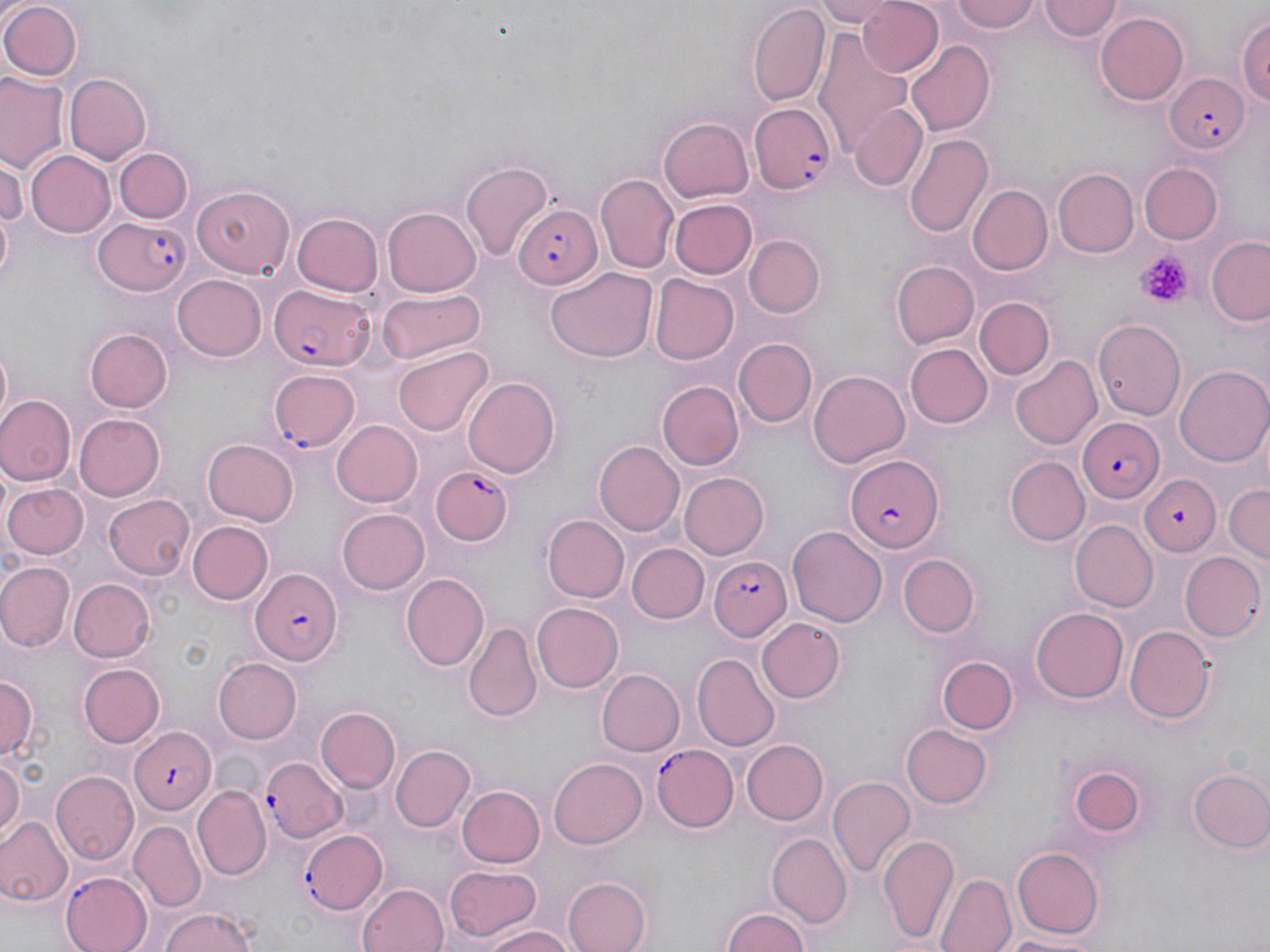 Approximate bounding boxes as (x1, y1, x2, y2) in pixels. Plasmodium falciparum-infected red blood cell locations: (1165, 71, 1251, 156), (750, 102, 837, 196), (512, 203, 600, 289), (93, 217, 191, 296), (270, 286, 373, 370), (268, 369, 361, 451), (1075, 415, 1164, 501), (843, 453, 945, 553), (428, 464, 514, 548), (710, 557, 793, 642), (248, 566, 340, 666), (126, 726, 217, 815), (650, 743, 739, 833), (263, 756, 349, 842), (298, 827, 389, 915). Uninfected red blood cell locations: (812, 0, 899, 26), (855, 0, 943, 77), (947, 0, 1040, 35), (1036, 0, 1124, 41), (0, 1, 81, 82), (747, 4, 831, 107), (1238, 12, 1270, 114), (1094, 13, 1190, 105), (814, 32, 911, 157), (905, 39, 995, 135), (0, 73, 66, 173), (64, 73, 150, 165), (849, 103, 926, 192), (659, 115, 754, 204), (904, 133, 994, 240), (112, 144, 192, 226), (26, 150, 115, 237), (0, 157, 25, 232), (461, 161, 553, 261), (1138, 163, 1223, 245), (1055, 168, 1139, 258), (596, 173, 679, 274), (192, 183, 297, 278), (966, 184, 1054, 276), (669, 199, 756, 279), (382, 207, 483, 295), (294, 213, 383, 297), (744, 235, 826, 317), (1207, 236, 1270, 326), (892, 260, 978, 349), (545, 267, 658, 363), (649, 272, 739, 365), (171, 273, 265, 361), (378, 287, 486, 364), (974, 296, 1053, 381), (1093, 318, 1187, 422), (85, 327, 172, 413), (733, 338, 817, 428), (1, 339, 14, 429), (906, 344, 993, 428), (392, 347, 491, 437), (1010, 355, 1101, 450), (1175, 366, 1270, 467), (811, 369, 908, 468), (462, 375, 562, 478), (659, 380, 742, 469), (0, 396, 75, 485), (74, 412, 164, 499), (333, 421, 421, 507), (202, 437, 298, 525), (595, 440, 685, 537), (1007, 456, 1091, 545), (678, 471, 769, 559), (1138, 475, 1223, 557), (2, 483, 88, 560), (1225, 483, 1269, 562), (105, 493, 196, 580), (336, 508, 430, 595), (543, 515, 627, 603), (187, 520, 272, 605), (1071, 520, 1157, 611), (788, 525, 887, 627), (629, 543, 708, 624), (1182, 551, 1266, 641), (900, 554, 977, 637), (0, 563, 74, 651), (400, 573, 489, 672), (69, 579, 155, 661), (532, 602, 624, 692), (1032, 605, 1130, 701), (756, 617, 847, 703), (462, 621, 542, 724), (1123, 625, 1215, 726), (692, 653, 780, 749), (937, 653, 1019, 734), (213, 657, 303, 743), (78, 662, 165, 747), (596, 669, 684, 756), (0, 672, 39, 760), (316, 707, 400, 794), (901, 723, 992, 808), (741, 738, 828, 825), (391, 744, 477, 830), (0, 756, 23, 842), (547, 757, 646, 850), (1068, 765, 1149, 839), (1188, 769, 1270, 854), (53, 771, 141, 865), (829, 777, 917, 879), (456, 785, 543, 869), (194, 786, 270, 880), (1, 817, 71, 906), (130, 821, 206, 913), (877, 832, 960, 943), (769, 833, 852, 928), (1010, 847, 1106, 940), (445, 863, 546, 945), (61, 871, 153, 952), (935, 874, 1016, 952), (564, 876, 651, 952), (358, 882, 448, 952), (156, 907, 261, 952), (720, 908, 814, 952), (480, 927, 574, 952), (998, 931, 1113, 950). Platelet locations: (1135, 252, 1191, 305). Slide-level diagnosis: Plasmodium falciparum. 1000x magnification. May-Grünwald-Giemsa-stained preparation. Image is 1270×952 pixels. One field of a larger specimen. Thin blood smear. Optical microscopy.